Report the malaria status of this cell.
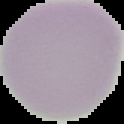

Uninfected.

Image is 124×124 pixels. Cell region segmented out of the field of view; the surrounding area is masked to black. From a thin blood smear.